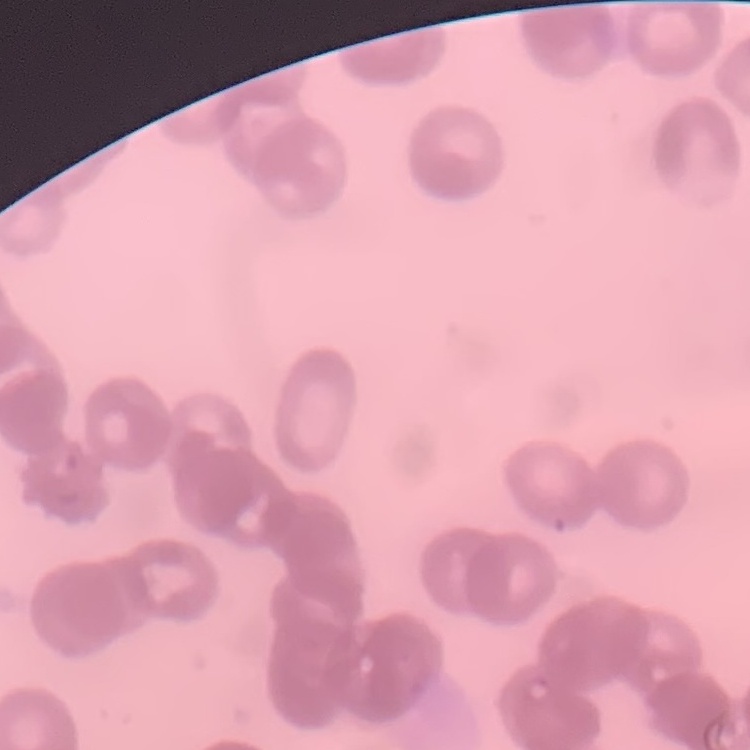

red blood cell morphology = rouleaux formation
preparation = thin blood smear
image type = one tile cut from a larger photomicrograph
stain = Field's or Giemsa